Assess this cell for malaria.
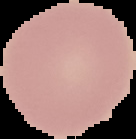
Uninfected.

Segmented cell region on a black background. Image is 136×139 pixels. From a thin blood smear.